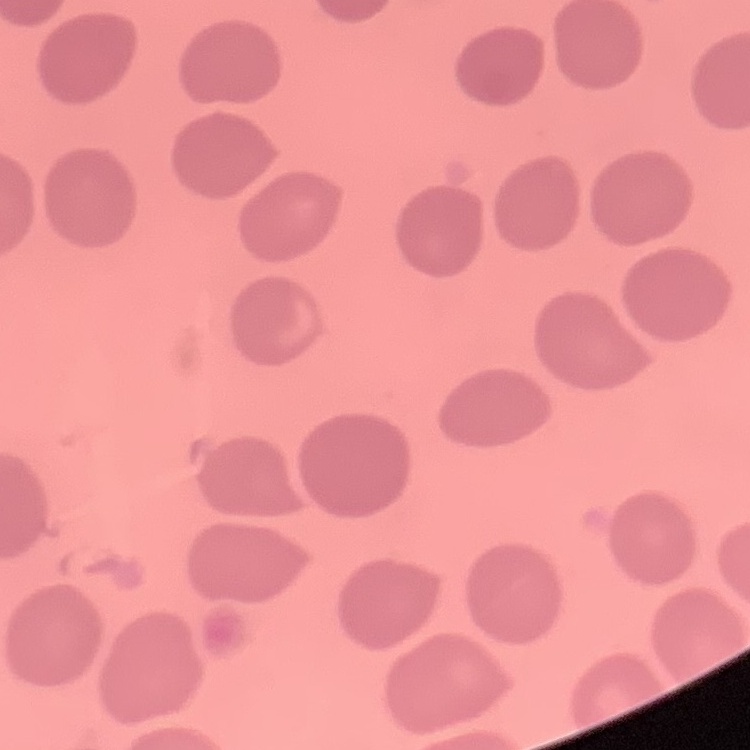
{
  "erythrocyte_morphology": "no rouleaux formation",
  "image_type": "one tile cut from a larger photomicrograph",
  "stain": "Field's or Giemsa",
  "preparation": "thin blood film"
}